Assess the morphology of the red blood cells.
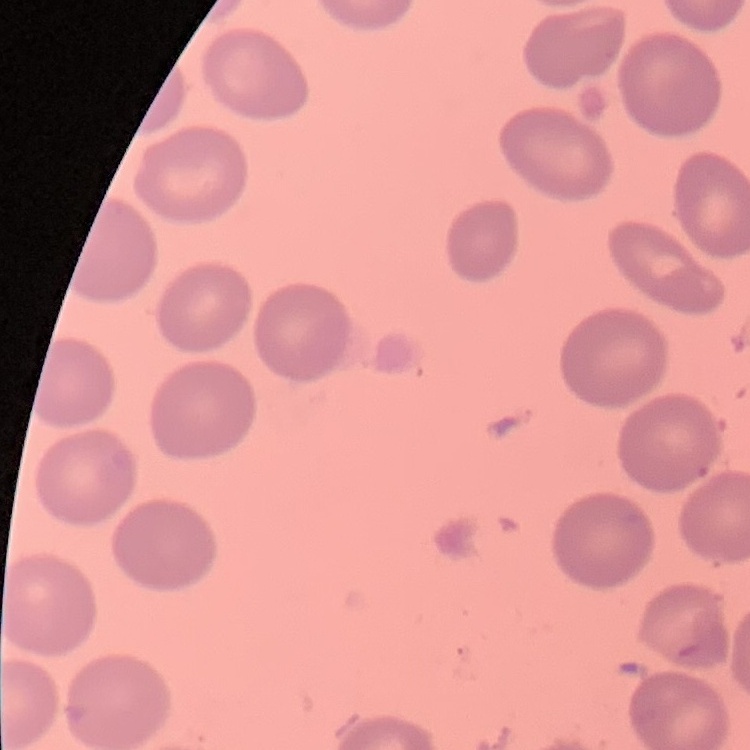
No rouleaux formation.

One tile cut from a larger photomicrograph. Field's or Giemsa stain. Thin peripheral smear.